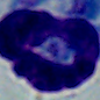
Summary:
  - Identification: leukocyte
  - Modality: micrograph
  - Magnification: 1000x